Describe the morphology of the erythrocytes.
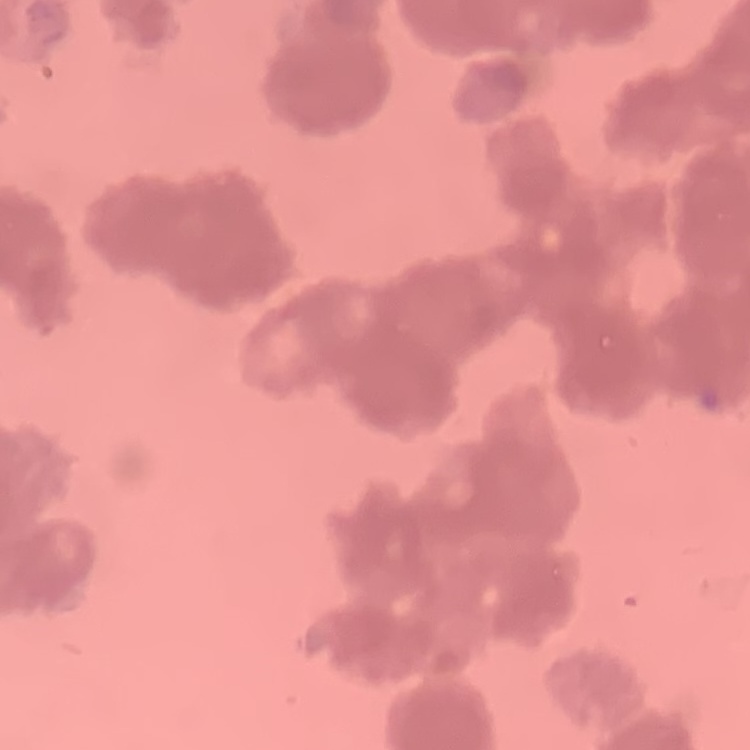

Rouleaux formation.

Stained with either Field's or Giemsa. Thin blood film. Square crop of a larger photomicrograph.